Give the extent of all uninfected red blood cells.
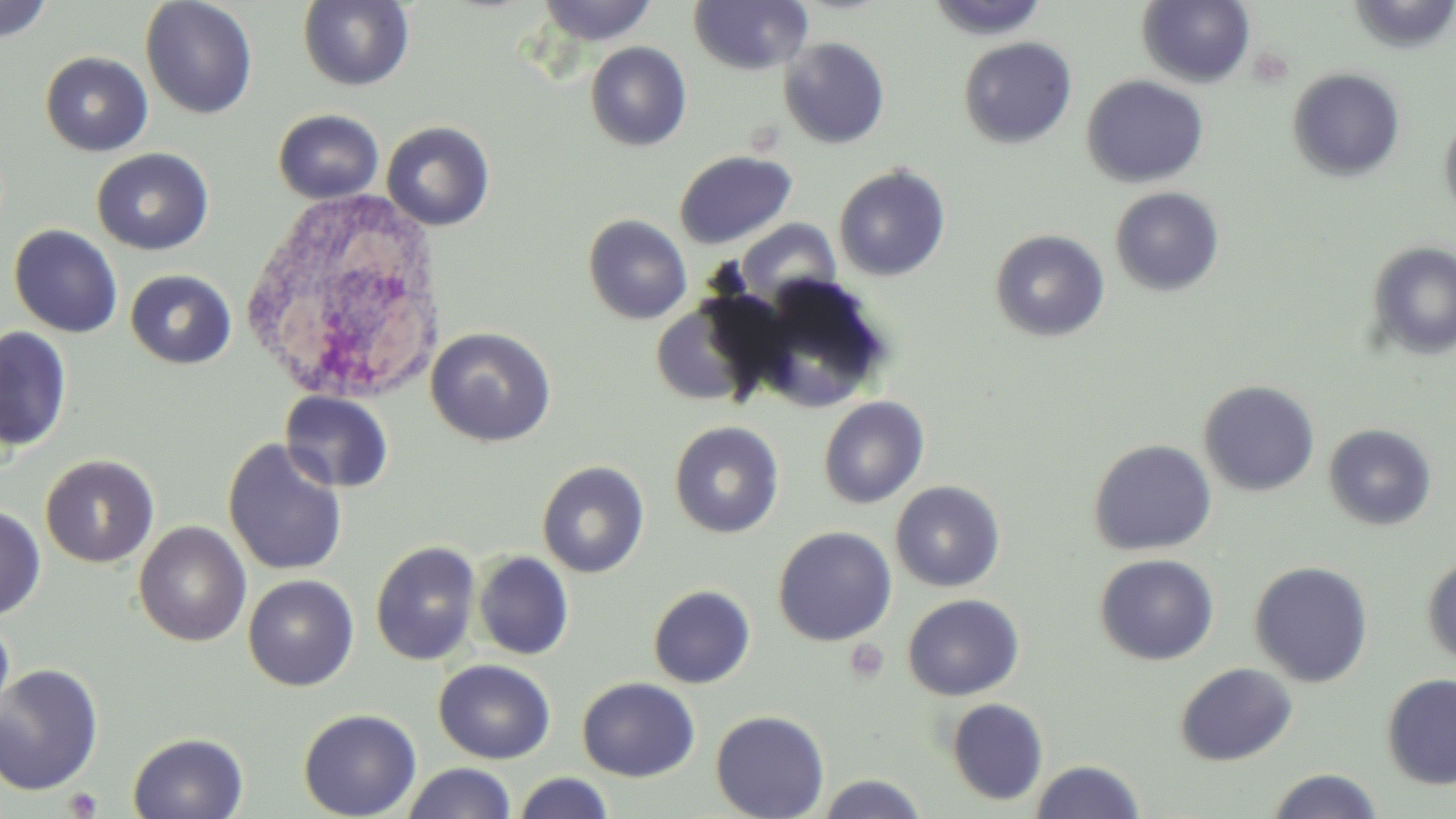
Approximate bounding boxes as (x1,y1)-(x2,y2) corner pairs in pixels.
Uninfected red blood cells: (140,0)-(258,119), (535,0)-(657,45), (689,0)-(813,75), (926,0)-(1050,40), (1137,0)-(1256,88), (0,1)-(55,43), (298,1)-(415,91), (958,36)-(1077,149), (778,37)-(890,148), (585,42)-(692,151), (40,52)-(153,157), (1287,67)-(1406,182), (1082,75)-(1208,188), (273,109)-(384,204), (1439,114)-(1456,223), (381,121)-(495,231), (92,148)-(213,255), (674,151)-(796,249), (833,164)-(951,281), (1109,186)-(1225,296), (583,214)-(692,324), (737,220)-(840,303), (9,224)-(123,338), (990,229)-(1110,342), (1367,241)-(1456,360), (125,269)-(236,369), (752,280)-(891,413), (650,296)-(778,408), (0,326)-(72,451), (425,326)-(556,447), (1198,379)-(1320,496), (280,390)-(394,493), (818,396)-(930,508), (669,421)-(784,538), (1323,423)-(1437,531), (222,438)-(349,577), (1088,439)-(1217,556), (40,454)-(159,568), (537,460)-(650,578), (890,481)-(1005,592), (0,504)-(45,619), (134,521)-(251,647), (773,526)-(896,645), (370,540)-(481,666), (473,551)-(574,660), (1095,553)-(1219,665), (1422,554)-(1456,669), (1249,560)-(1374,688), (242,574)-(359,691), (648,585)-(755,689), (902,594)-(1024,700), (0,613)-(15,726), (433,659)-(555,764), (1175,662)-(1297,766), (0,664)-(104,796), (1381,673)-(1456,790), (577,677)-(700,782), (946,698)-(1049,805), (298,708)-(421,819), (711,710)-(829,819), (127,732)-(249,819), (1029,759)-(1145,819), (401,762)-(517,819), (1265,768)-(1384,819), (512,771)-(615,819), (815,773)-(929,819).

Platelet locations: (844,639)-(890,684), (62,788)-(104,818). White blood cell locations: (240,185)-(448,405). Slide-level diagnosis: negative for blood parasites. One field of a larger specimen. Image is 1456×819 pixels. May-Grünwald-Giemsa stain. Light microscopy. Captured at 1000x magnification. Thin blood film.